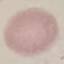

malaria status = uninfected
image type = automatically extracted cell patch, resized to 64 × 64 pixels
preparation = thin smear
stain = Giemsa
capture = smartphone through the microscope eyepiece